Assess this cell for malaria.
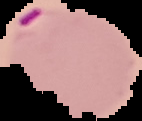
Parasitized.

{
  "image_type": "segmented cell region on a black background",
  "image_size": "142×121 pixels",
  "preparation": "thin blood smear"
}